Outline each blood parasite and name the species.
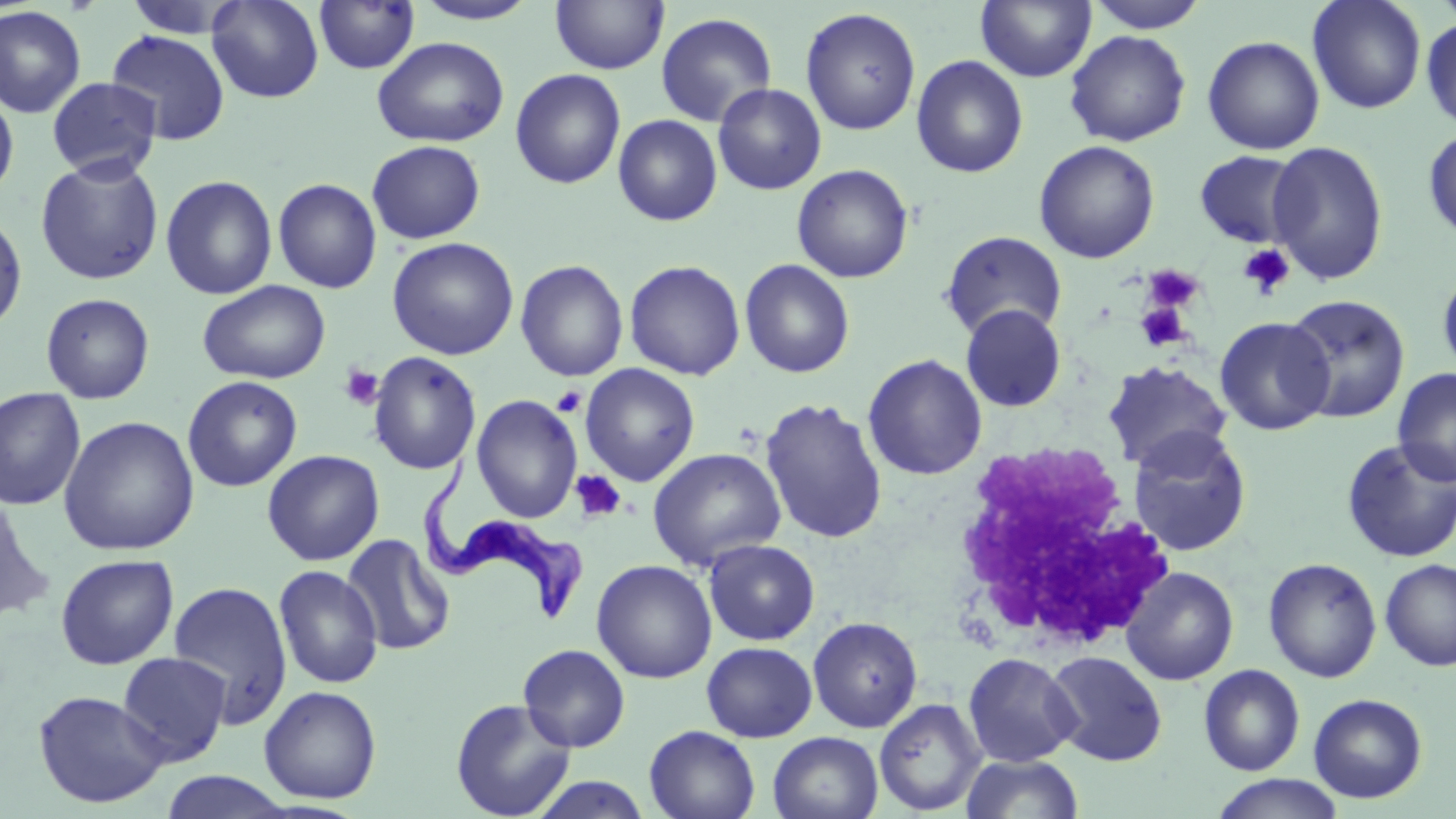

Approximate bounding boxes as [x1, y1, x2, y2] in pixels.
Trypanosoma brucei: [420, 454, 582, 625].
No Plasmodium falciparum, Plasmodium ovale, Plasmodium malariae, Plasmodium vivax, or Babesia divergens observed.

{
  "slide_level_diagnosis": "Trypanosoma brucei",
  "field_of_view": "one of a larger specimen",
  "uninfected_red_blood_cell_locations": "approximate bounding boxes as [x1, y1, x2, y2] in pixels: [120, 0, 247, 39], [207, 0, 324, 103], [313, 0, 420, 75], [411, 0, 542, 25], [550, 0, 669, 75], [1085, 0, 1209, 33], [1307, 0, 1427, 114], [976, 1, 1096, 82], [0, 5, 87, 119], [800, 7, 922, 136], [655, 12, 778, 127], [1421, 16, 1456, 135], [107, 29, 230, 145], [1065, 30, 1191, 147], [1202, 35, 1325, 155], [371, 36, 509, 147], [911, 55, 1028, 177], [510, 69, 626, 189], [47, 77, 162, 181], [713, 83, 827, 194], [0, 87, 19, 201], [613, 115, 723, 226], [1422, 125, 1455, 246], [366, 140, 486, 244], [1033, 140, 1161, 263], [1266, 140, 1389, 285], [1193, 150, 1305, 248], [35, 155, 164, 285], [791, 163, 914, 283], [160, 175, 278, 300], [272, 178, 382, 294], [0, 208, 28, 335], [940, 230, 1067, 341], [386, 237, 519, 360], [514, 259, 629, 382], [739, 259, 855, 378], [624, 260, 746, 380], [1437, 265, 1456, 384], [198, 279, 330, 385], [40, 293, 155, 405], [1283, 294, 1411, 423], [958, 302, 1068, 413], [1214, 316, 1335, 435], [367, 351, 482, 475], [863, 353, 988, 481], [1101, 360, 1233, 472], [580, 363, 701, 486], [1392, 368, 1456, 486], [182, 375, 303, 492], [0, 387, 86, 511], [471, 394, 583, 524], [759, 397, 888, 544], [3, 398, 159, 546], [58, 415, 200, 556], [1128, 427, 1252, 556], [1341, 438, 1456, 562], [647, 447, 786, 571], [262, 449, 385, 566], [0, 488, 55, 626], [341, 533, 456, 656], [703, 539, 820, 646], [55, 553, 179, 669], [1263, 557, 1382, 682], [591, 559, 717, 683], [1379, 559, 1456, 671], [273, 564, 383, 689], [1121, 566, 1239, 685], [168, 580, 293, 728], [808, 616, 923, 733], [701, 641, 817, 742], [518, 643, 631, 752], [1044, 649, 1168, 766], [117, 652, 232, 767], [962, 652, 1081, 767], [1199, 664, 1305, 776], [259, 684, 382, 804], [33, 689, 169, 809], [1308, 693, 1428, 803], [874, 698, 987, 816], [450, 699, 576, 819], [644, 725, 761, 819], [768, 731, 883, 819], [960, 752, 1085, 818], [160, 770, 296, 818], [1209, 774, 1346, 819], [527, 775, 655, 818]",
  "preparation": "thin blood film",
  "stain": "May-Grünwald-Giemsa",
  "modality": "light microscopy",
  "magnification": "1000x",
  "image_size": "1456×819 pixels",
  "white_blood_cell_locations": "approximate bounding boxes as [x1, y1, x2, y2] in pixels: [947, 440, 1180, 656]",
  "platelet_locations": "approximate bounding boxes as [x1, y1, x2, y2] in pixels: [1238, 244, 1295, 298], [1142, 264, 1205, 315], [1135, 302, 1190, 352], [339, 365, 384, 410], [551, 386, 587, 418], [571, 469, 627, 523]"
}